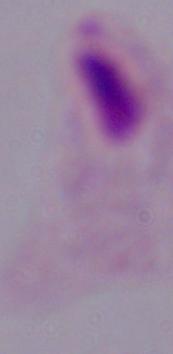
Summary:
  - Identification: trichomonad
  - Modality: micrograph
  - Magnification: 1000x